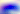
Captured at 400x magnification. Micrograph. Toxoplasma gondii is seen.